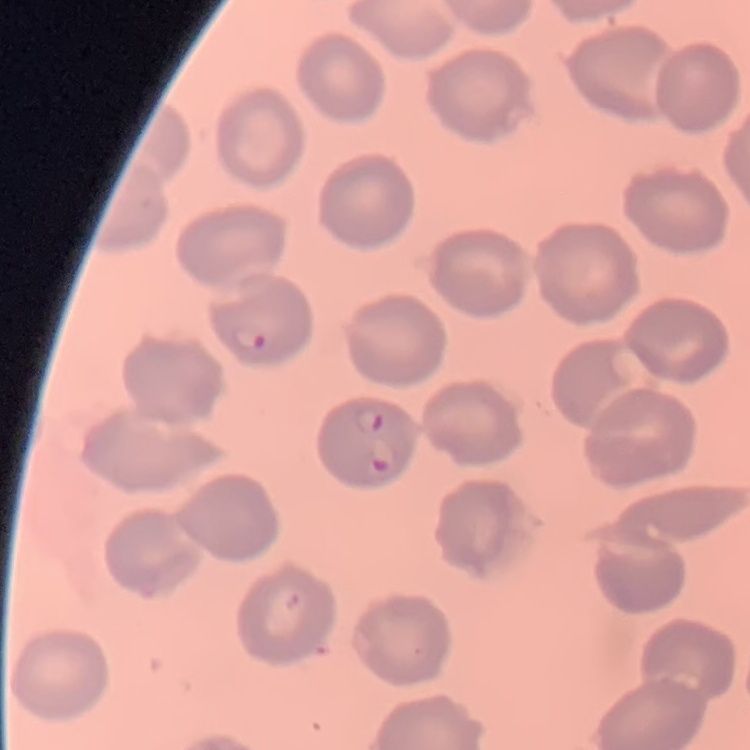

The red blood cells exhibit no rouleaux formation. Stained with either Field's or Giemsa. One tile cut from a larger photomicrograph. Thin blood film.